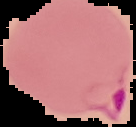 The area outside the segmented cell region is set to black. Image is 136×127 pixels. From a thin blood film. Result: Plasmodium parasites identified.